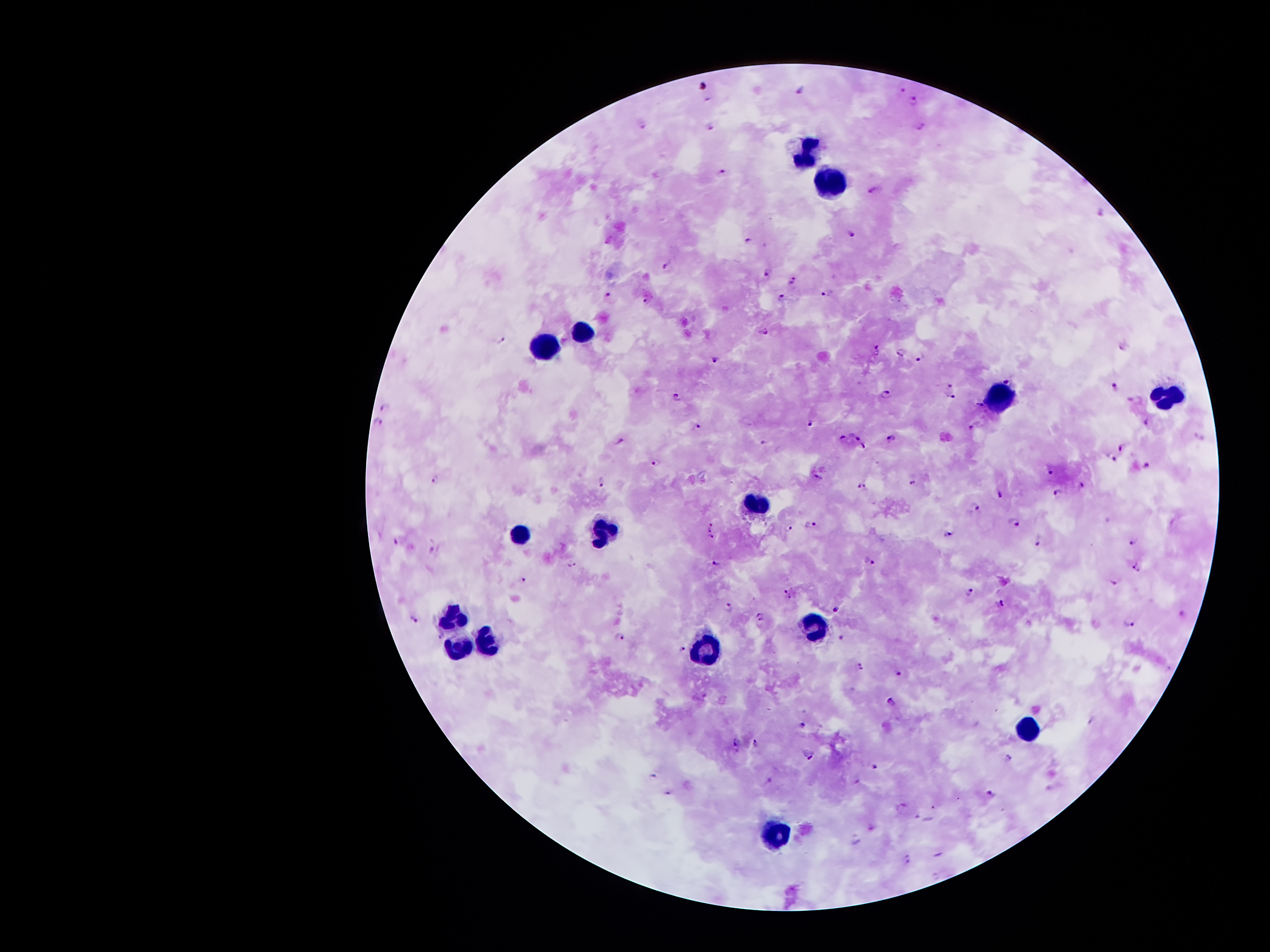
Approximate centers as (x, y) in pixels.
Summary:
  - Plasmodium parasite locations: (703, 83), (900, 88), (802, 90), (915, 101), (710, 125), (920, 129), (724, 171), (876, 188), (853, 234), (746, 240), (667, 266), (768, 274), (793, 279), (828, 294), (609, 295), (782, 297), (647, 300), (763, 333), (502, 340), (877, 347), (902, 351), (920, 356), (715, 358), (1007, 379), (950, 384), (1115, 385), (886, 393), (678, 397), (950, 397), (1135, 399), (979, 405), (383, 408), (1145, 420), (811, 423), (376, 424), (696, 424), (971, 427), (855, 433), (842, 438), (892, 439), (620, 440), (764, 442), (1122, 444), (864, 446), (1113, 456), (655, 461), (1146, 465), (1052, 469), (818, 475), (436, 479), (604, 482), (911, 482), (1082, 484), (862, 485), (1057, 490), (999, 494), (975, 506), (1013, 522), (713, 523), (810, 523), (789, 527), (711, 529), (949, 533), (710, 537), (1039, 540), (398, 541), (1133, 541), (432, 550), (716, 563), (867, 563), (572, 565), (1136, 568), (524, 579), (1115, 581), (969, 591), (789, 592), (1002, 603), (729, 605), (836, 609), (759, 617), (414, 618), (1130, 624), (843, 635), (619, 637), (682, 650), (861, 665), (899, 672), (891, 703), (801, 724), (738, 739), (755, 742), (808, 754), (1010, 758), (874, 765), (654, 776), (767, 781), (858, 781), (668, 792), (989, 792), (903, 804), (908, 860)
  - Leukocyte locations: (803, 149), (826, 182), (581, 332), (543, 342), (996, 393), (1174, 395), (755, 503), (606, 530), (523, 535), (456, 619), (813, 626), (491, 645), (463, 646), (706, 652), (1023, 729), (772, 835)
  - Preparation: thick blood smear
  - Stain: Giemsa
  - Capture: smartphone camera through the microscope eyepiece
  - Image size: 1270×952 pixels
  - Magnification: 100x
  - Patient malaria status: infected with Plasmodium falciparum
  - Field of view: one from this slide